Identify the cell.
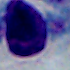

This is a leukocyte.

Summary:
  - Modality: photomicrograph
  - Magnification: 1000x